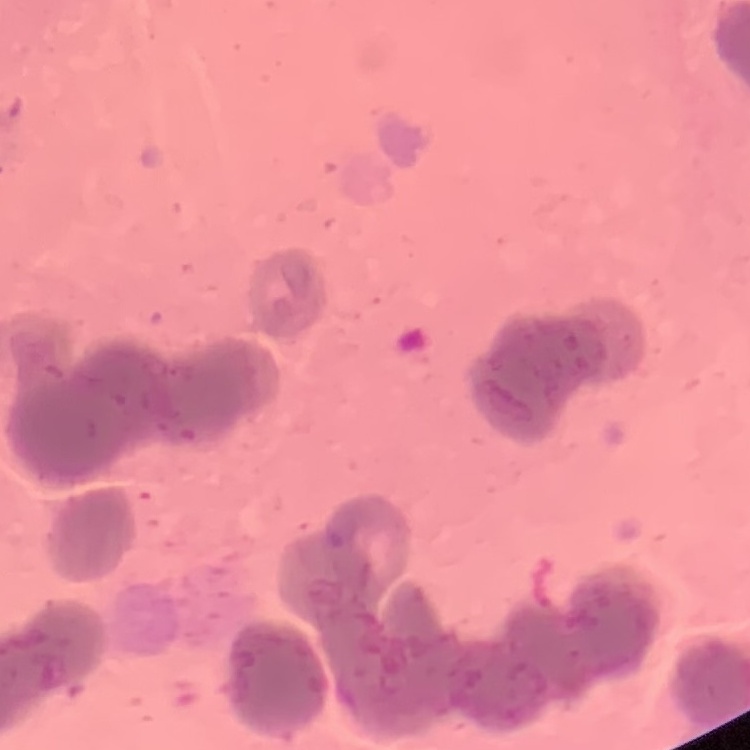

red blood cell morphology = rouleaux formation
image type = square crop of a larger photomicrograph
preparation = thin blood film
stain = Field's or Giemsa